Outline each blood parasite and name the species.
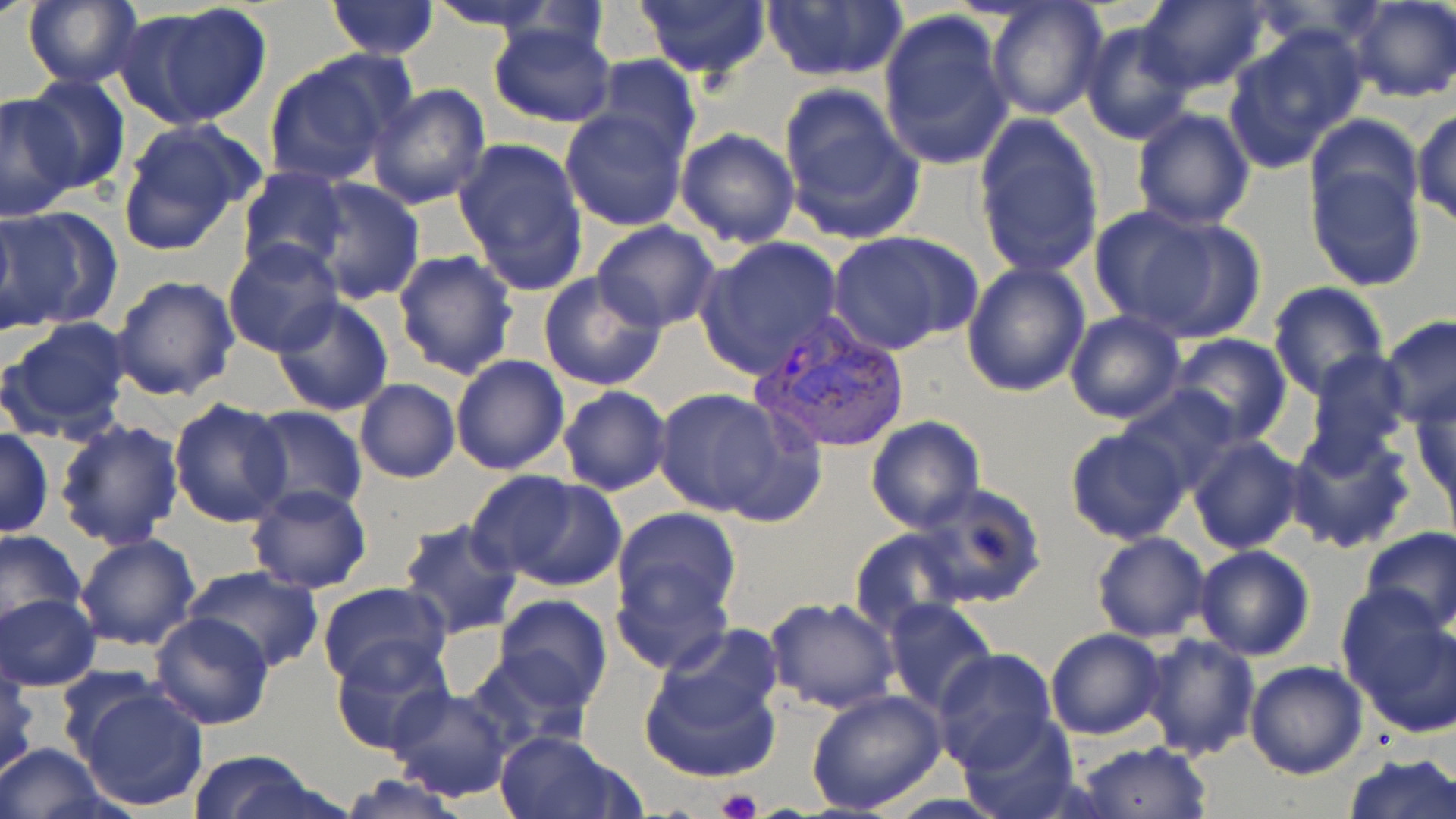
Approximate bounding boxes as (x1,y1)-(x2,y2) corner pairs in pixels.
Plasmodium vivax-infected red blood cells: (748,313)-(910,456).
No Plasmodium falciparum, Plasmodium ovale, Plasmodium malariae, Babesia divergens, or Trypanosoma brucei observed.

Platelet locations: (718,789)-(763,819). Uninfected red blood cell locations: (325,0)-(441,58), (424,0)-(570,33), (633,0)-(772,82), (760,0)-(907,84), (1135,0)-(1268,95), (21,1)-(143,88), (119,1)-(274,128), (984,1)-(1109,120), (1345,1)-(1455,104), (877,9)-(1015,172), (1078,17)-(1198,145), (486,20)-(619,128), (1224,28)-(1365,170), (263,52)-(411,188), (586,55)-(703,165), (22,74)-(132,196), (366,84)-(491,211), (776,84)-(926,245), (0,90)-(82,219), (1130,104)-(1257,230), (559,107)-(689,233), (1412,107)-(1456,228), (973,111)-(1106,280), (114,118)-(263,256), (674,126)-(800,248), (453,137)-(590,296), (1305,139)-(1428,292), (237,167)-(350,277), (306,177)-(425,305), (1097,204)-(1247,341), (0,208)-(117,333), (591,221)-(722,333), (828,231)-(978,356), (695,236)-(846,379), (222,240)-(345,358), (393,249)-(519,381), (961,259)-(1093,398), (538,270)-(667,392), (110,274)-(241,401), (1267,281)-(1389,397), (271,297)-(395,417), (1063,311)-(1186,425), (1379,313)-(1456,430), (2,316)-(134,442), (1166,334)-(1293,448), (1301,351)-(1412,470), (450,354)-(570,475), (354,379)-(460,483), (1120,385)-(1244,496), (557,386)-(670,496), (651,388)-(802,522), (1411,393)-(1456,513), (169,397)-(293,527), (247,405)-(368,517), (866,417)-(985,533), (55,418)-(185,551), (0,426)-(54,538), (1064,426)-(1192,546), (1284,427)-(1418,553), (1187,435)-(1305,554), (468,468)-(627,592), (912,483)-(1046,610), (246,484)-(373,595), (611,507)-(742,644), (396,519)-(526,640), (1359,525)-(1456,634), (850,526)-(969,635), (0,528)-(86,635), (1090,530)-(1212,642), (75,533)-(201,652), (1193,545)-(1316,661), (182,565)-(326,673), (315,581)-(451,689), (0,593)-(100,689), (1341,593)-(1456,731), (492,595)-(614,711), (763,598)-(900,714), (883,598)-(997,717), (148,612)-(275,730), (1045,628)-(1167,739), (637,629)-(788,785), (1135,631)-(1261,758), (331,641)-(451,757), (931,649)-(1058,773), (1243,660)-(1368,779), (55,665)-(166,761), (0,667)-(38,778), (73,683)-(210,812), (384,685)-(515,801), (807,688)-(947,815), (955,712)-(1080,819), (493,729)-(640,819), (1075,741)-(1212,818), (0,743)-(112,818), (186,750)-(322,817), (1343,751)-(1456,819), (333,773)-(475,819). Slide-level diagnosis: Plasmodium vivax. Captured at 1000x magnification. Single field of view. Image is 1456×819 pixels. Thin blood film. Optical microscopy. May-Grünwald-Giemsa-stained preparation.